State the blood parasite species.
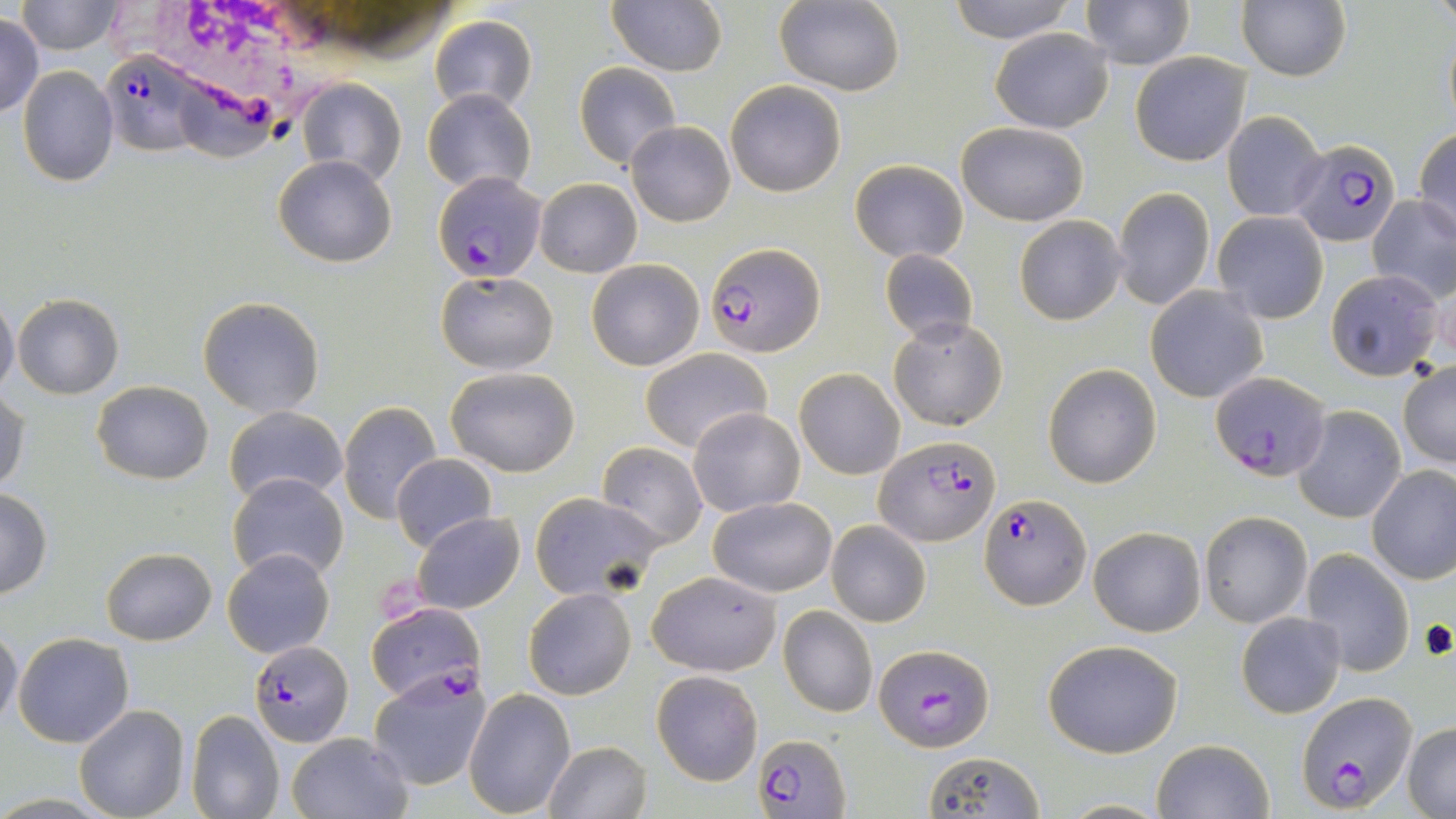

Plasmodium falciparum.

Summary:
  - Coordinate format: approximate bounding boxes as named x1/y1/x2/y2 corners in pixels
  - Plasmodium falciparum-infected red blood cell locations: (x1=101, y1=51, x2=215, y2=157), (x1=1288, y1=136, x2=1402, y2=247), (x1=434, y1=170, x2=547, y2=282), (x1=706, y1=241, x2=825, y2=359), (x1=1211, y1=374, x2=1326, y2=481), (x1=874, y1=436, x2=1002, y2=548), (x1=979, y1=493, x2=1090, y2=609), (x1=365, y1=602, x2=484, y2=705), (x1=249, y1=643, x2=352, y2=746), (x1=875, y1=643, x2=993, y2=749), (x1=1296, y1=690, x2=1417, y2=810), (x1=752, y1=735, x2=850, y2=817)
  - White blood cell locations: (x1=118, y1=0, x2=369, y2=101)
  - Uninfected red blood cell locations: (x1=944, y1=0, x2=1078, y2=43), (x1=1080, y1=0, x2=1194, y2=69), (x1=16, y1=1, x2=126, y2=54), (x1=775, y1=1, x2=905, y2=96), (x1=607, y1=2, x2=727, y2=77), (x1=1237, y1=2, x2=1350, y2=81), (x1=429, y1=15, x2=536, y2=117), (x1=0, y1=16, x2=45, y2=118), (x1=992, y1=28, x2=1112, y2=133), (x1=1129, y1=51, x2=1252, y2=166), (x1=575, y1=63, x2=680, y2=168), (x1=17, y1=67, x2=119, y2=186), (x1=296, y1=78, x2=406, y2=189), (x1=726, y1=80, x2=845, y2=196), (x1=422, y1=87, x2=536, y2=196), (x1=1222, y1=110, x2=1329, y2=223), (x1=626, y1=120, x2=736, y2=227), (x1=957, y1=121, x2=1088, y2=226), (x1=1413, y1=127, x2=1456, y2=244), (x1=273, y1=155, x2=397, y2=268), (x1=849, y1=160, x2=968, y2=263), (x1=534, y1=177, x2=641, y2=278), (x1=1112, y1=187, x2=1215, y2=311), (x1=1367, y1=195, x2=1456, y2=305), (x1=1211, y1=212, x2=1329, y2=324), (x1=1014, y1=214, x2=1127, y2=325), (x1=880, y1=249, x2=979, y2=344), (x1=587, y1=259, x2=705, y2=371), (x1=435, y1=270, x2=557, y2=373), (x1=1324, y1=271, x2=1444, y2=381), (x1=1145, y1=285, x2=1270, y2=403), (x1=13, y1=293, x2=123, y2=399), (x1=197, y1=296, x2=325, y2=418), (x1=0, y1=297, x2=19, y2=399), (x1=890, y1=317, x2=1007, y2=430), (x1=640, y1=349, x2=772, y2=454), (x1=1398, y1=358, x2=1456, y2=468), (x1=1043, y1=364, x2=1161, y2=487), (x1=445, y1=366, x2=581, y2=477), (x1=794, y1=367, x2=904, y2=480), (x1=92, y1=381, x2=213, y2=484), (x1=0, y1=385, x2=28, y2=495), (x1=338, y1=400, x2=443, y2=526), (x1=223, y1=405, x2=349, y2=506), (x1=1293, y1=405, x2=1406, y2=523), (x1=689, y1=407, x2=805, y2=517), (x1=596, y1=441, x2=707, y2=549), (x1=391, y1=455, x2=496, y2=552), (x1=1368, y1=465, x2=1456, y2=584), (x1=226, y1=473, x2=349, y2=586), (x1=1325, y1=484, x2=1436, y2=639), (x1=0, y1=489, x2=52, y2=599), (x1=529, y1=492, x2=662, y2=600), (x1=708, y1=496, x2=837, y2=597), (x1=1200, y1=510, x2=1312, y2=627), (x1=410, y1=512, x2=525, y2=614), (x1=826, y1=520, x2=930, y2=627), (x1=1088, y1=527, x2=1205, y2=636), (x1=102, y1=546, x2=216, y2=645), (x1=223, y1=548, x2=335, y2=657), (x1=1300, y1=549, x2=1414, y2=677), (x1=647, y1=570, x2=783, y2=676), (x1=523, y1=587, x2=636, y2=700), (x1=779, y1=606, x2=877, y2=718), (x1=1236, y1=612, x2=1345, y2=717), (x1=0, y1=627, x2=23, y2=732), (x1=14, y1=632, x2=133, y2=748), (x1=1042, y1=639, x2=1185, y2=757), (x1=367, y1=669, x2=491, y2=791), (x1=651, y1=671, x2=763, y2=786), (x1=463, y1=688, x2=574, y2=815), (x1=76, y1=705, x2=189, y2=819), (x1=186, y1=710, x2=285, y2=819), (x1=1402, y1=723, x2=1456, y2=816), (x1=286, y1=731, x2=412, y2=819), (x1=1151, y1=738, x2=1273, y2=819), (x1=544, y1=740, x2=651, y2=819), (x1=922, y1=750, x2=1048, y2=817), (x1=1057, y1=799, x2=1175, y2=817)
  - Stain: May-Grünwald-Giemsa
  - Field of view: one of a larger specimen
  - Preparation: thin blood smear
  - Image size: 1456×819 pixels
  - Magnification: 1000x
  - Modality: light microscopy